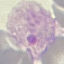

Result: malaria parasites detected. Photographed with a smartphone camera at the microscope eyepiece. Cell patch, automatically extracted from a larger field of view and resized to 64 × 64 pixels. Giemsa-stained preparation. Thin blood film.